Identify the preparation type.
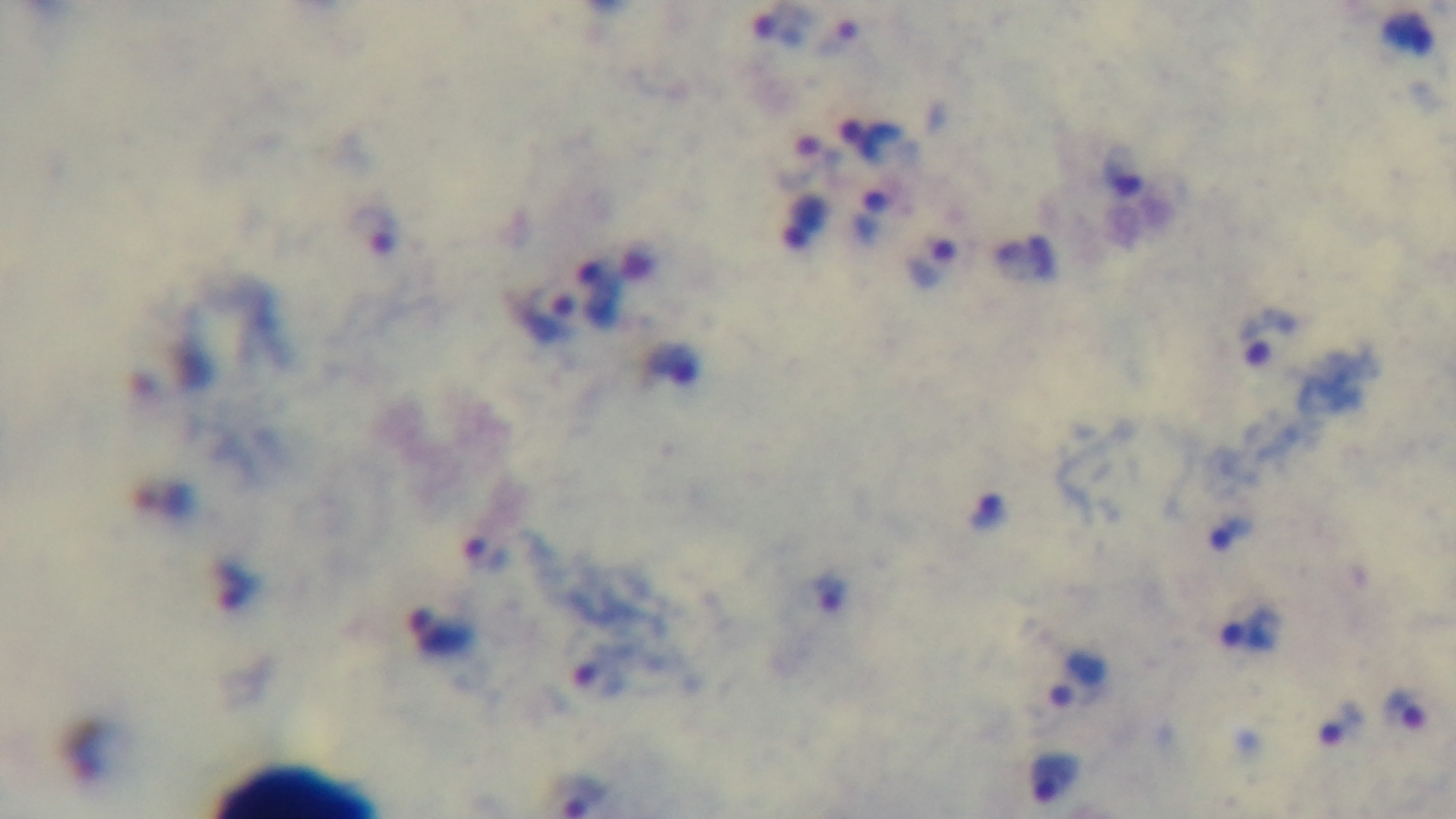

It is a thick blood film.

Summary:
  - Field of view: single
  - Malaria status: positive
  - Capture: mounted 4K digital camera
  - Stain: Giemsa
  - Modality: light microscopy
  - Objective: 100x oil immersion